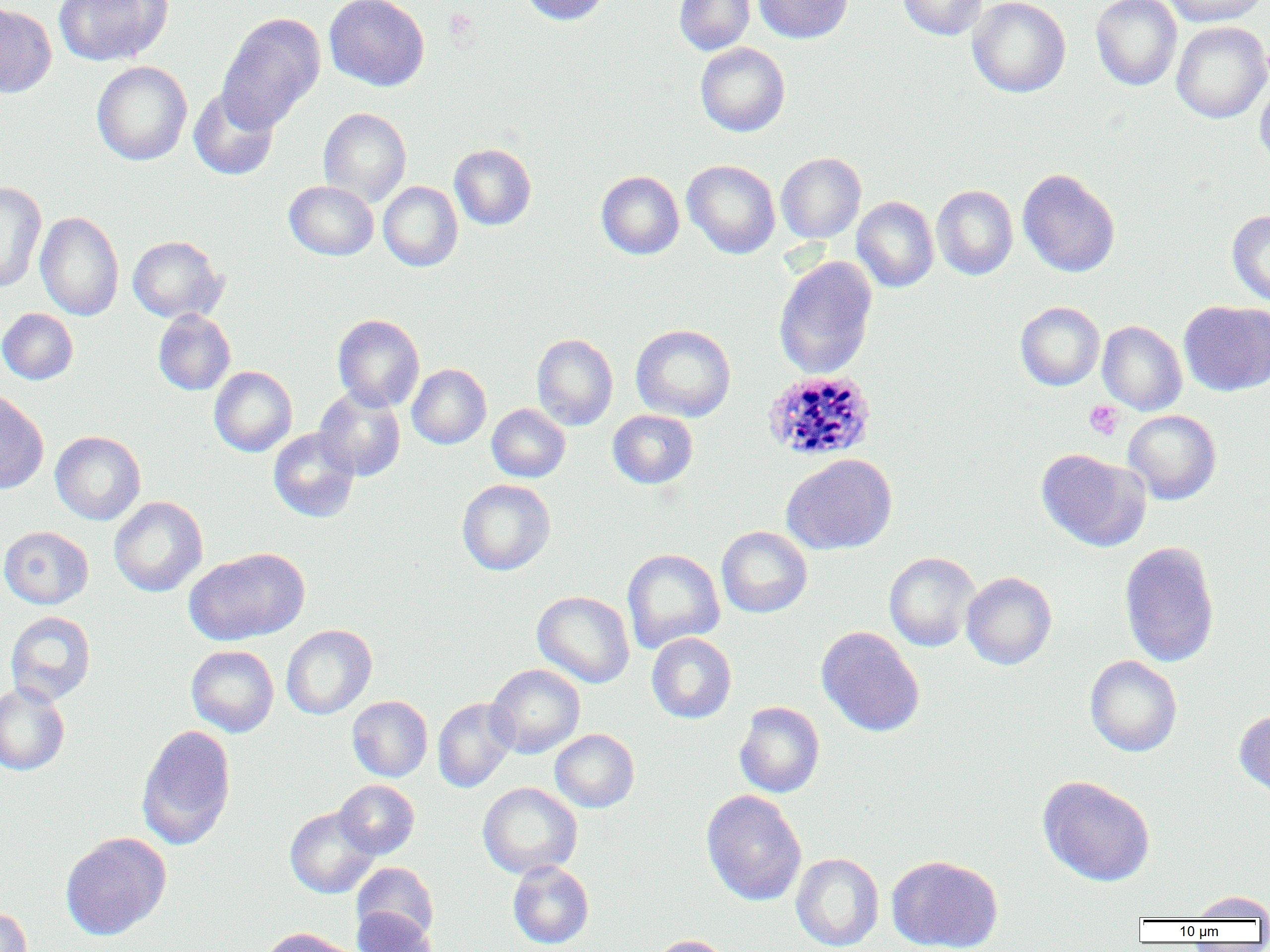 Approximate bounding boxes as (x1, y1, x2, y2) in pixels. Uninfected red blood cell locations: (54, 0, 172, 66), (324, 0, 430, 91), (520, 0, 610, 26), (674, 0, 756, 56), (754, 0, 853, 43), (898, 0, 987, 40), (967, 0, 1070, 97), (1090, 0, 1182, 91), (1165, 0, 1266, 26), (0, 4, 57, 98), (217, 13, 325, 131), (1171, 21, 1270, 124), (695, 42, 790, 136), (91, 61, 192, 165), (1255, 76, 1270, 171), (189, 87, 279, 181), (318, 107, 411, 206), (449, 143, 536, 230), (776, 152, 866, 244), (682, 160, 781, 259), (1017, 169, 1121, 277), (596, 171, 684, 260), (0, 181, 46, 293), (284, 181, 379, 260), (378, 181, 463, 272), (931, 185, 1018, 280), (852, 196, 939, 292), (1227, 209, 1270, 307), (35, 211, 124, 321), (127, 235, 226, 323), (773, 256, 877, 379), (1179, 300, 1270, 396), (1015, 301, 1104, 391), (0, 308, 78, 384), (153, 309, 235, 395), (332, 314, 424, 411), (1097, 321, 1187, 415), (631, 324, 736, 422), (532, 333, 618, 430), (407, 364, 491, 449), (209, 366, 297, 457), (314, 386, 406, 482), (0, 389, 49, 494), (487, 403, 570, 482), (608, 410, 698, 489), (1123, 410, 1221, 504), (268, 428, 360, 522), (50, 431, 146, 525), (1037, 449, 1150, 551), (781, 454, 897, 555), (456, 479, 555, 576), (108, 496, 208, 597), (0, 526, 93, 609), (716, 526, 813, 618), (1119, 540, 1220, 668), (185, 547, 310, 645), (622, 548, 725, 654), (884, 552, 981, 651), (961, 571, 1057, 670), (532, 590, 635, 688), (5, 611, 96, 706), (281, 624, 377, 719), (816, 626, 925, 737), (646, 632, 737, 723), (186, 645, 279, 737), (1084, 655, 1182, 757), (486, 664, 585, 758), (0, 682, 70, 775), (347, 696, 433, 782), (432, 698, 519, 793), (734, 701, 825, 798), (1235, 709, 1270, 801), (136, 725, 237, 850), (550, 729, 639, 812), (1037, 775, 1156, 886), (335, 780, 419, 859), (478, 782, 582, 878), (701, 790, 806, 906), (285, 806, 379, 898), (60, 832, 171, 940), (790, 853, 884, 951), (886, 855, 1003, 952), (508, 861, 594, 949), (352, 862, 439, 942), (1188, 890, 1270, 921), (0, 906, 31, 952), (351, 908, 438, 952), (259, 928, 355, 952), (649, 935, 731, 952). Platelet locations: (1084, 400, 1124, 440). Plasmodium vivax-infected red blood cell locations: (762, 370, 877, 462). Slide-level diagnosis: Plasmodium vivax. Image is 1270×952 pixels. Light microscopy. Thin blood smear. Single field of view. Captured at 1000x magnification.